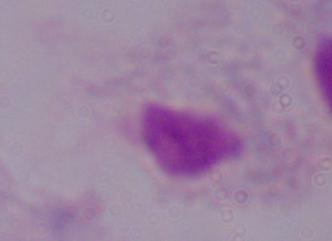
identification = trichomonad
modality = micrograph
magnification = 1000x